Assess this cell for malaria.
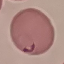
Parasitized.

Automatically extracted cell patch, resized to 64 × 64 pixels. Photographed with a smartphone camera at the microscope eyepiece. Thin smear of blood. Giemsa stain.